Report the malaria status of this cell.
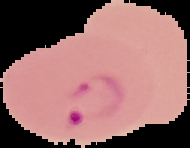
Parasitized.

preparation = thin blood film
image size = 190×148 pixels
image type = segmented cell region with the area outside set to black